Name the parasite shown.
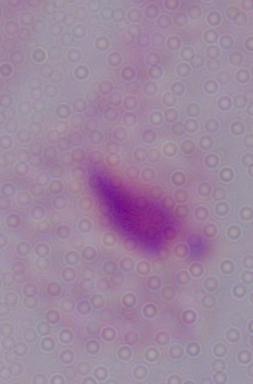

This is a trichomonad.

Summary:
  - Magnification: 1000x
  - Modality: micrograph